Report the malaria status of this cell.
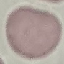

It is uninfected.

capture = smartphone camera at the microscope eyepiece
image type = automatically extracted cell patch, resized to 64 × 64 pixels
preparation = thin blood smear
stain = Giemsa